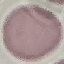
Result: no malaria parasites seen. Photographed with a smartphone camera at the microscope eyepiece. Thin smear of blood. Cell patch, automatically extracted from a larger field of view and resized to 64 × 64 pixels. Giemsa-stained preparation.